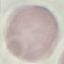

Malaria status: uninfected. Cell patch, automatically extracted from a larger field of view and resized to 64 × 64 pixels. Thin blood film. Acquired by smartphone through the microscope eyepiece. Giemsa stain.